Locate every leukocyte (white blood cell).
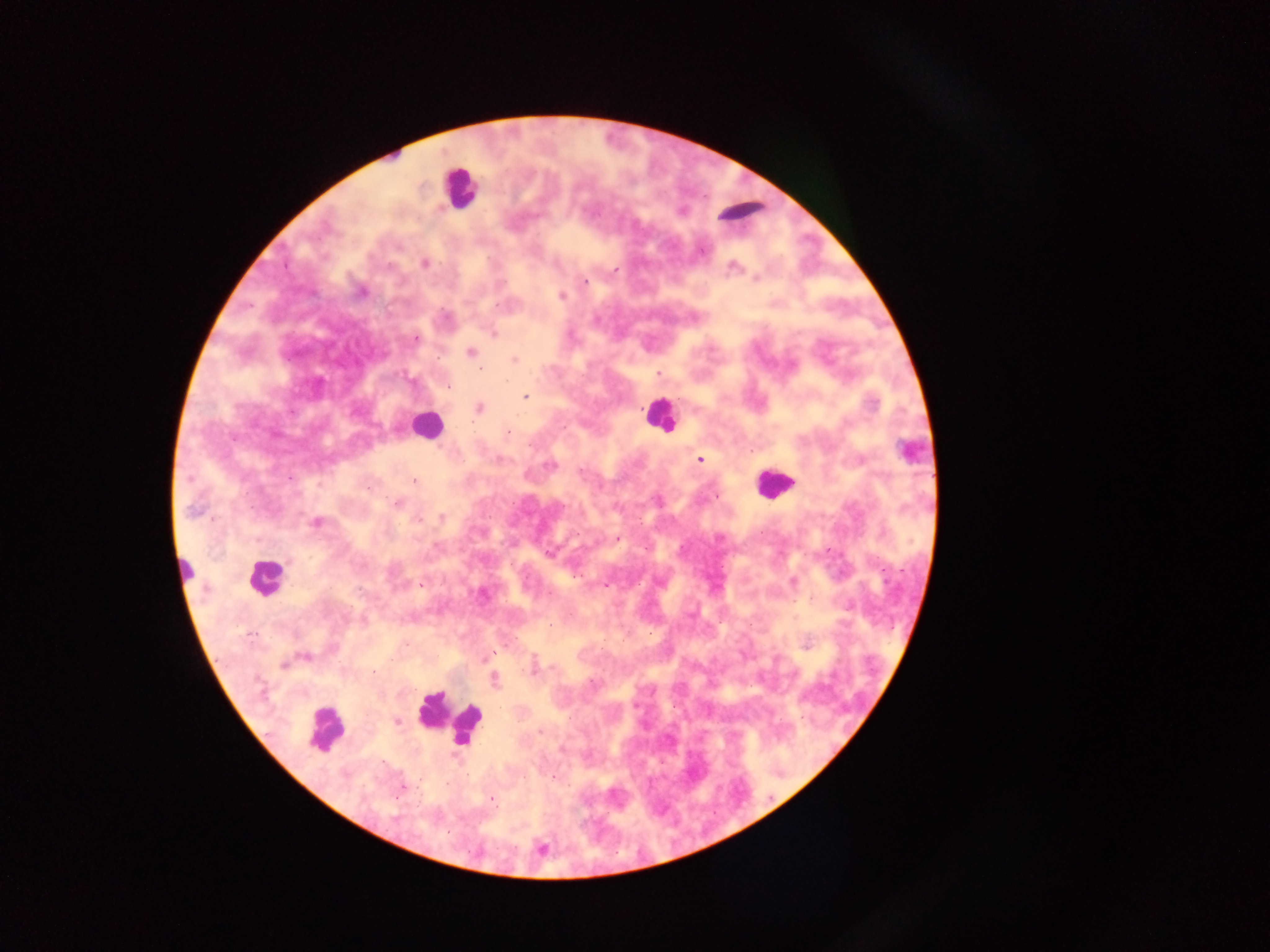

Approximate centers as [x, y] in pixels.
Leukocytes: [459, 188], [744, 211], [659, 415], [425, 425], [909, 450], [773, 483], [186, 572], [265, 577], [446, 718], [323, 729].

Malaria parasite locations: [424, 263], [733, 266], [615, 270], [756, 279], [584, 281], [361, 292], [561, 296], [494, 333], [415, 339], [471, 352], [514, 359], [658, 374], [448, 386], [525, 397], [480, 407], [508, 433], [699, 460], [550, 465], [414, 481], [715, 497], [397, 504], [193, 510], [441, 517], [418, 520], [316, 523], [617, 539], [646, 549], [550, 554], [793, 581], [421, 585], [605, 585], [359, 590], [361, 620], [550, 624], [406, 643], [494, 654], [490, 656], [305, 657], [283, 665], [550, 667], [373, 672], [495, 680], [592, 683], [396, 721], [540, 732], [554, 777], [401, 787], [492, 799]. Collected in Ghana. Thick blood smear. Photographed through a microscope with a mobile-phone camera. Image is 1270×952 pixels. One field of view.